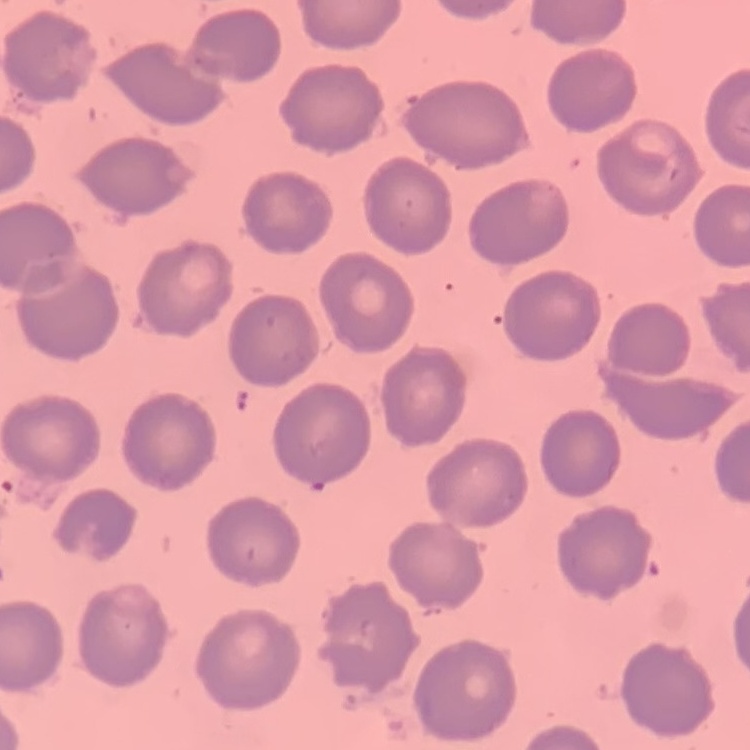 The erythrocytes exhibit no rouleaux formation. Stained with either Field's or Giemsa. Thin blood film. One tile cut from a larger photomicrograph.